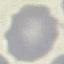

malaria status = uninfected
image type = cell patch, automatically extracted from a larger field of view and resized to 64 × 64 pixels
preparation = thin blood film
capture = smartphone camera at the microscope eyepiece
stain = Giemsa